Report the malaria status of this cell.
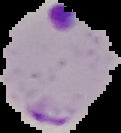
It is parasitized.

Summary:
  - Preparation: thin blood film
  - Image type: cell region segmented out of the field of view; surrounding area masked to black
  - Image size: 121×133 pixels